Describe the morphology of the erythrocytes.
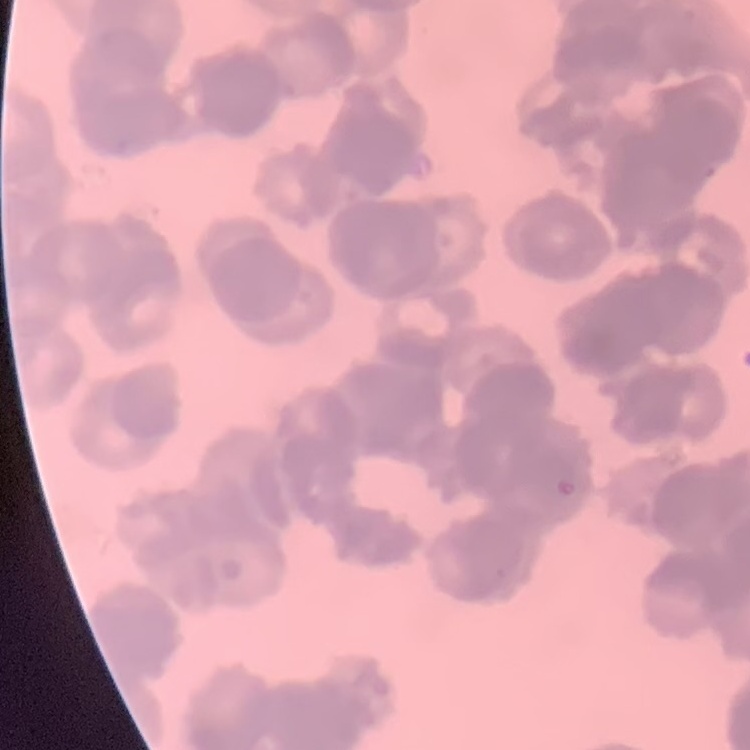

They show rouleaux formation.

image type = one tile cut from a larger photomicrograph
stain = Field's or Giemsa
preparation = thin blood smear